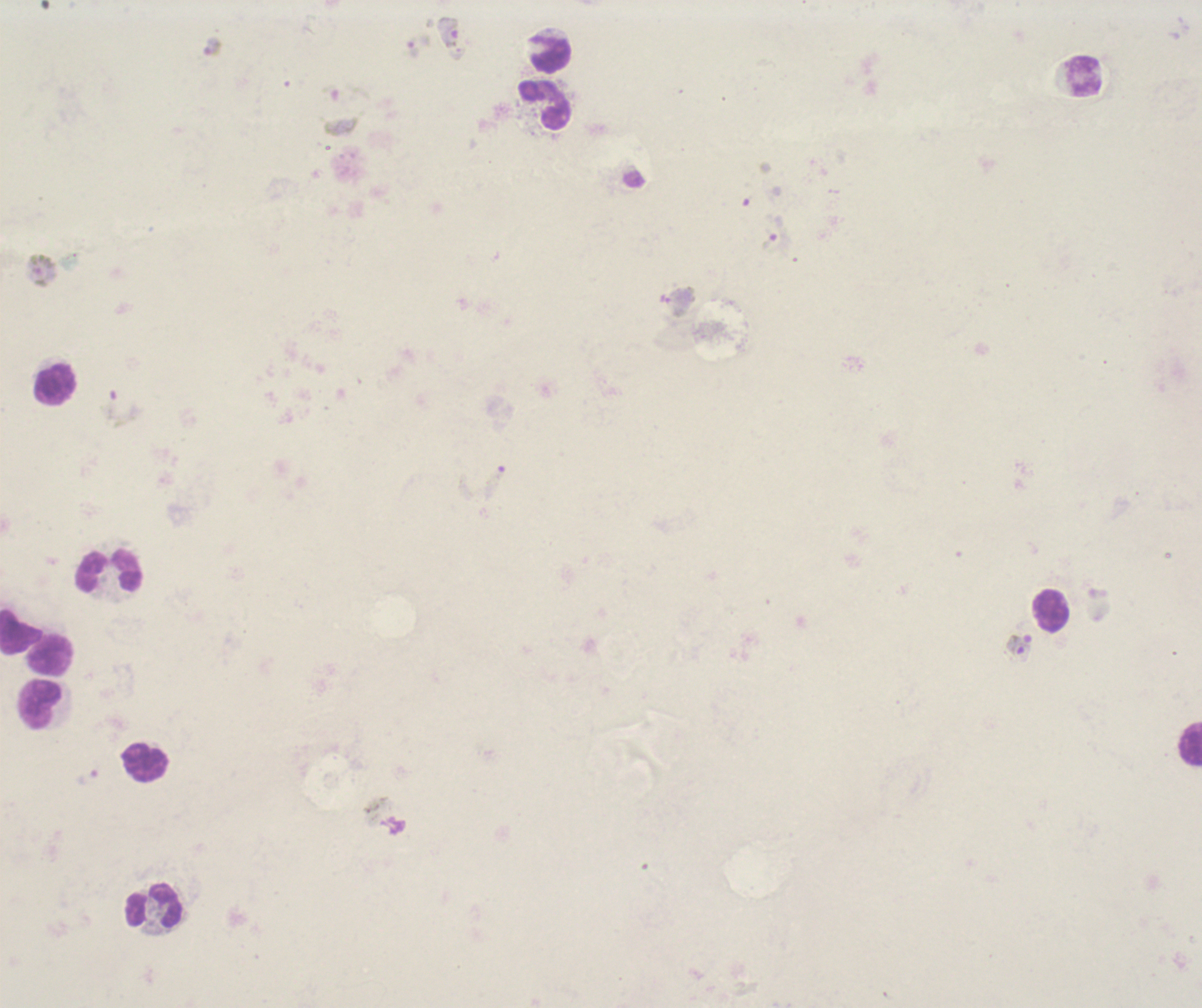

coordinate format = approximate centers as (x, y) in pixels
trophozoite locations = (213, 46), (777, 237)
gametocyte locations = (448, 33), (344, 108), (41, 271), (1020, 648), (386, 817)
schizont locations = (125, 408)
leukocyte locations = (550, 54), (1084, 77), (545, 105), (55, 385), (109, 572), (1050, 611), (21, 632), (49, 653), (41, 704), (1189, 744), (145, 762), (154, 906)
life-cycle stages observed = trophozoite, schizont, gametocyte
stain = Romanowsky
field of view = one from this slide
background quality = unsatisfactory
image size = 1202×1008 pixels
context = previously used in an actual diagnosis
coloration quality = bad
magnification = 100x
result = positive for malaria parasites
preparation = thick smear of blood